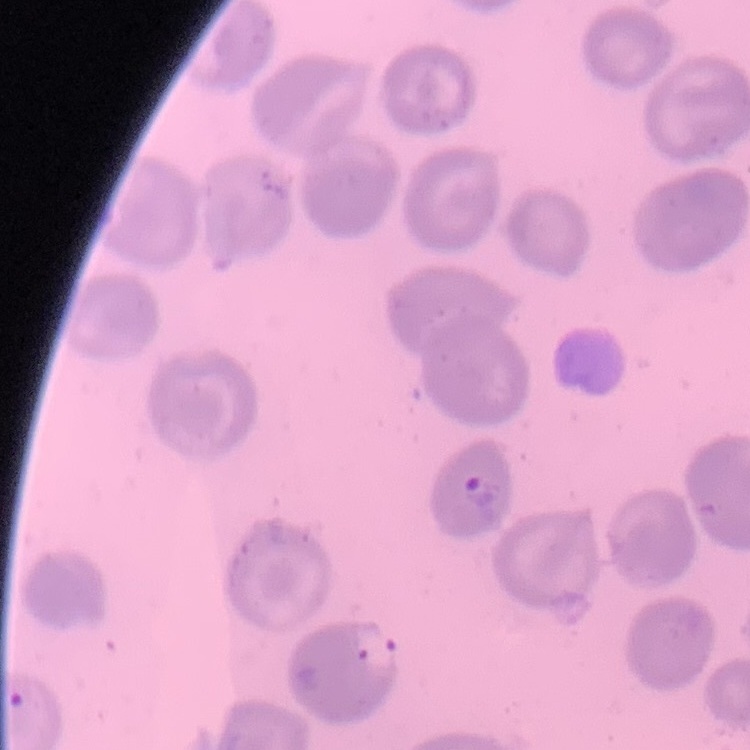

Summary:
  - Red blood cell morphology: no rouleaux formation
  - Preparation: thin blood film
  - Stain: Field's or Giemsa
  - Image type: square crop of a larger photomicrograph